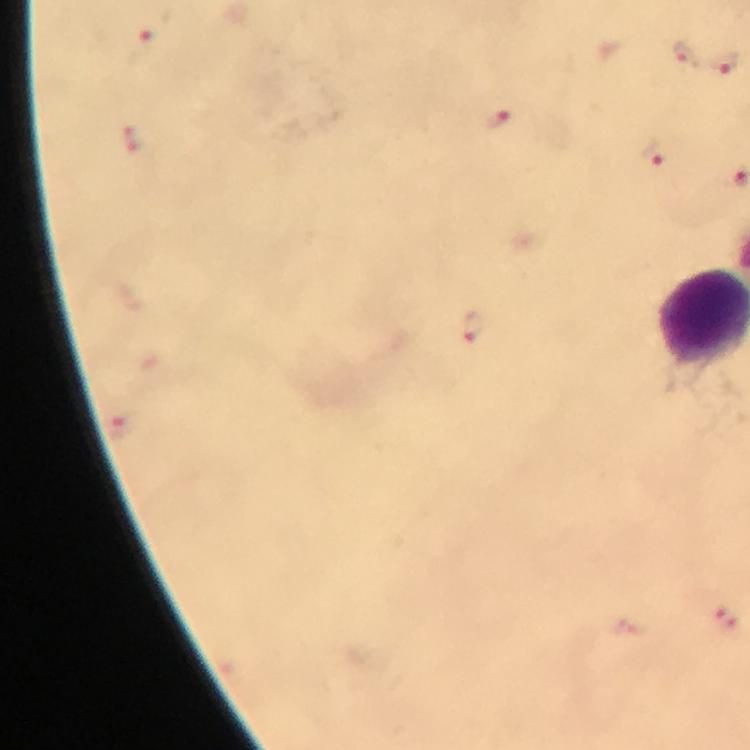

context = from a diagnostic examination for malaria
magnification = 100x
cropped from = one field of view
image size = 750×750 pixels
stain = Giemsa
Plasmodium parasite locations = approximate centers as [x, y] in pixels: [147, 37], [684, 53], [723, 63], [495, 119], [131, 138], [653, 151], [472, 327], [725, 619]
immersion oil = applied
preparation = thick blood smear
capture = smartphone photograph through a microscope